Identify the parasite.
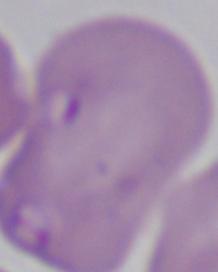
Babesia.

1000x magnification. Photomicrograph.